Give the extent of all Plasmodium falciparum-infected red blood cells.
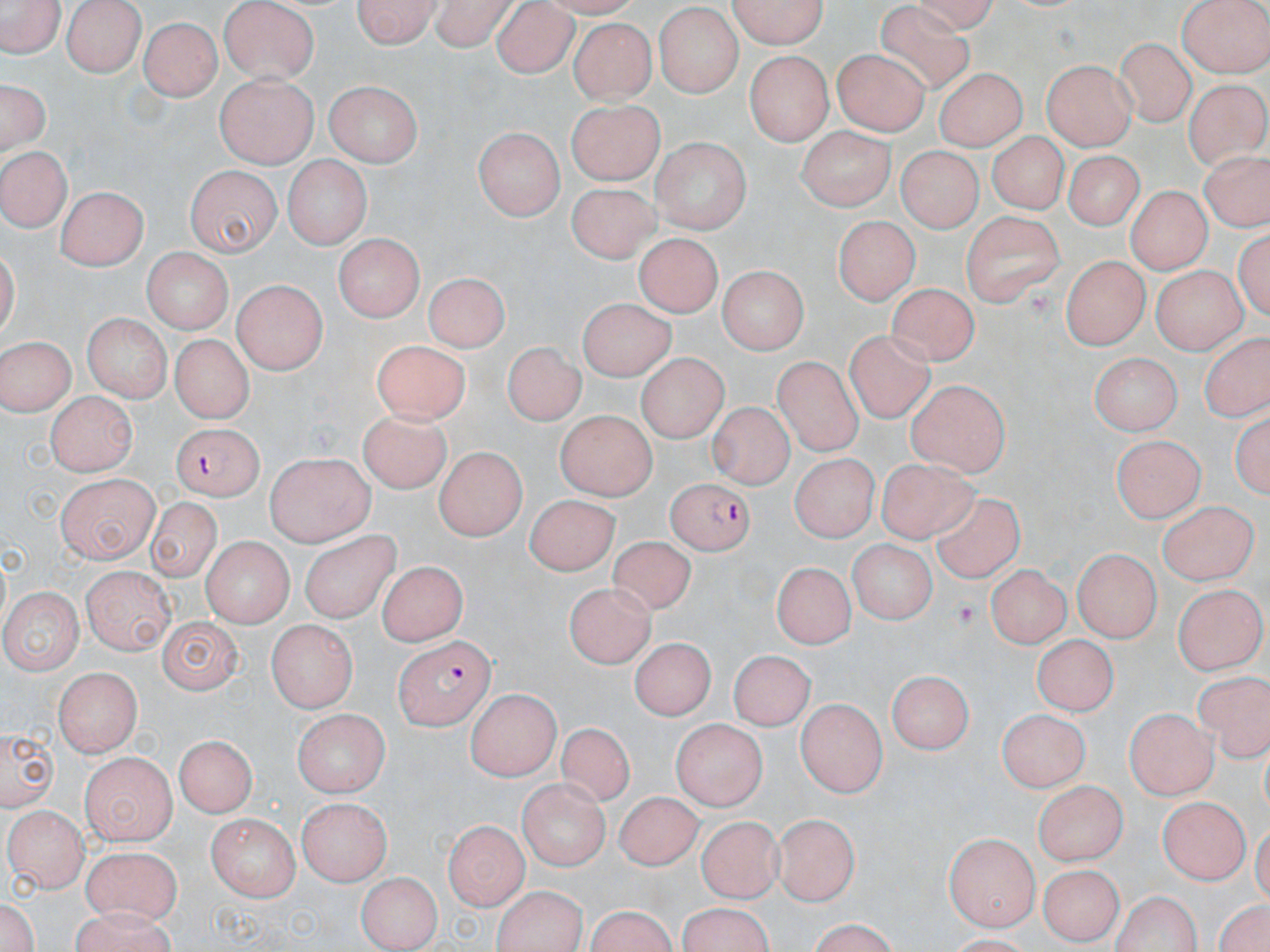
Approximate bounding boxes as (x1,y1)-(x2,y2) corner pairs in pixels.
Plasmodium falciparum-infected red blood cells: (168,420)-(268,494), (667,478)-(754,554), (393,636)-(492,731).

Platelet locations: (950,601)-(983,630). Uninfected red blood cell locations: (62,0)-(147,76), (353,0)-(438,50), (428,0)-(517,49), (731,0)-(832,51), (1178,0)-(1270,77), (219,1)-(322,83), (1,2)-(64,59), (492,4)-(578,78), (653,5)-(744,97), (141,16)-(221,99), (568,17)-(654,102), (1114,37)-(1196,129), (833,46)-(931,134), (742,50)-(833,143), (1043,58)-(1136,148), (933,66)-(1026,149), (216,74)-(316,167), (1,78)-(51,158), (326,78)-(423,165), (1181,78)-(1270,167), (567,101)-(663,186), (798,126)-(892,207), (474,128)-(565,223), (991,132)-(1066,214), (652,136)-(752,233), (896,141)-(983,227), (1,144)-(73,231), (1061,150)-(1148,228), (284,155)-(369,251), (185,166)-(278,256), (565,182)-(660,261), (1125,185)-(1209,274), (56,187)-(143,270), (961,211)-(1065,307), (836,213)-(916,305), (638,232)-(721,314), (334,233)-(425,318), (140,249)-(232,334), (1059,254)-(1147,348), (715,259)-(808,351), (1151,260)-(1245,354), (424,268)-(509,347), (232,278)-(326,376), (890,281)-(975,368), (577,294)-(675,382), (83,313)-(172,400), (170,332)-(253,419), (846,332)-(938,426), (0,335)-(75,415), (503,340)-(584,423), (369,342)-(467,425), (1091,350)-(1180,437), (772,355)-(870,454), (635,356)-(730,442), (907,382)-(1009,478), (45,391)-(136,476), (708,403)-(800,489), (354,405)-(452,497), (1231,408)-(1268,505), (555,411)-(655,502), (1112,434)-(1203,524), (432,449)-(526,540), (263,452)-(374,547), (787,454)-(877,544), (880,459)-(983,545), (58,476)-(158,564), (522,494)-(615,576), (932,495)-(1034,588), (146,499)-(221,585), (1156,500)-(1254,585), (298,531)-(394,620), (202,535)-(292,627), (609,537)-(699,617), (843,540)-(935,620), (1073,548)-(1159,644), (774,561)-(854,647), (376,562)-(468,644), (988,565)-(1068,649), (83,568)-(174,653), (566,581)-(652,668), (1175,585)-(1266,676), (2,587)-(80,677), (156,615)-(243,695), (264,619)-(359,711), (1032,635)-(1115,715), (631,637)-(711,722), (732,648)-(813,726), (54,669)-(142,757), (887,669)-(974,756), (1196,673)-(1270,763), (467,692)-(557,783), (798,700)-(888,797), (996,705)-(1088,793), (1125,705)-(1216,800), (291,707)-(390,794), (670,718)-(768,806), (2,725)-(57,811), (553,725)-(632,809), (171,737)-(255,819), (94,750)-(242,827), (81,754)-(176,842), (518,778)-(608,873), (1033,779)-(1129,866), (613,791)-(702,868), (1152,797)-(1246,884), (294,798)-(391,886), (6,803)-(88,890), (778,810)-(861,905), (207,815)-(300,900), (695,817)-(779,904), (443,821)-(523,910), (944,830)-(1036,930), (79,845)-(180,924), (1037,864)-(1127,942), (359,870)-(440,948), (491,888)-(585,952), (1110,891)-(1208,952), (586,895)-(675,952), (1213,896)-(1270,952), (679,898)-(772,952), (66,913)-(181,952), (797,921)-(906,950). Slide-level diagnosis: Plasmodium falciparum. 1000x magnification. May-Grünwald-Giemsa stain. Single field of view. Optical microscopy. Thin blood smear. Image is 1270×952 pixels.